Give the extent of all Plasmodium vivax-infected red blood cells.
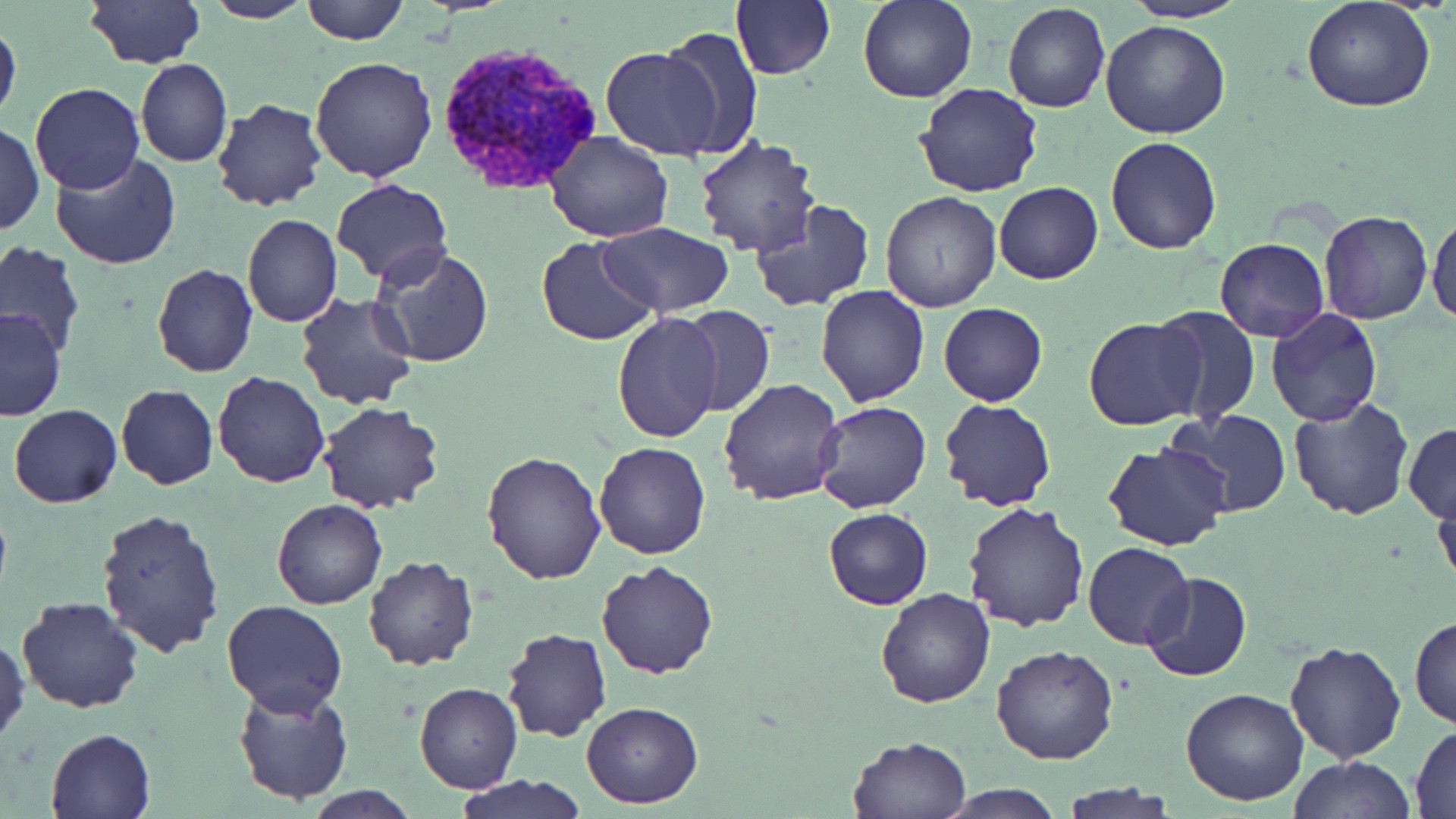

Approximate bounding boxes as (x1,y1)-(x2,y2) corner pairs in pixels.
Plasmodium vivax-infected red blood cells: (443,42)-(603,193).

Uninfected red blood cell locations: (83,0)-(203,69), (201,0)-(313,24), (301,0)-(409,45), (858,0)-(978,105), (1122,0)-(1247,22), (731,1)-(836,79), (1002,1)-(1110,114), (1302,1)-(1436,112), (0,19)-(21,124), (1099,19)-(1230,140), (659,28)-(763,156), (600,50)-(721,159), (310,57)-(438,183), (135,58)-(233,167), (28,83)-(146,194), (915,84)-(1045,198), (210,98)-(328,211), (0,121)-(44,236), (544,130)-(673,242), (1105,136)-(1223,255), (693,137)-(822,259), (51,154)-(184,272), (331,181)-(452,285), (995,182)-(1103,285), (881,192)-(1003,311), (749,201)-(876,313), (1427,210)-(1456,327), (1319,212)-(1434,325), (241,213)-(344,328), (598,222)-(732,316), (1215,237)-(1328,341), (536,238)-(659,345), (1,243)-(84,355), (367,247)-(495,368), (151,263)-(258,379), (816,286)-(929,405), (295,291)-(420,410), (938,302)-(1047,407), (679,305)-(775,417), (1149,305)-(1262,425), (1266,308)-(1382,427), (0,309)-(66,421), (610,313)-(726,444), (1083,317)-(1205,430), (212,370)-(330,489), (718,377)-(846,504), (116,384)-(219,490), (1288,396)-(1415,519), (938,399)-(1055,511), (811,400)-(930,514), (318,401)-(444,514), (9,403)-(122,508), (1162,411)-(1293,517), (1404,421)-(1456,522), (591,441)-(711,559), (1102,442)-(1230,551), (480,449)-(607,584), (1432,480)-(1455,595), (270,499)-(387,611), (963,500)-(1092,632), (96,507)-(226,656), (823,507)-(932,611), (1084,543)-(1193,650), (362,555)-(479,671), (596,560)-(720,679), (1139,571)-(1253,682), (877,588)-(996,708), (17,597)-(143,713), (220,601)-(347,717), (1409,616)-(1456,728), (500,630)-(612,743), (0,632)-(27,746), (1285,639)-(1406,765), (990,643)-(1120,765), (414,682)-(522,794), (233,683)-(354,805), (1180,688)-(1310,806), (581,701)-(703,809), (1411,725)-(1456,817), (45,727)-(157,818), (846,734)-(972,819), (1290,754)-(1415,818), (456,774)-(587,819), (1059,782)-(1181,818), (306,784)-(421,818), (937,784)-(1069,819). Slide-level diagnosis: Plasmodium vivax. Single field of view. Image is 1456×819 pixels. 1000x magnification. Thin blood smear. May-Grünwald-Giemsa-stained preparation. Light microscopy.